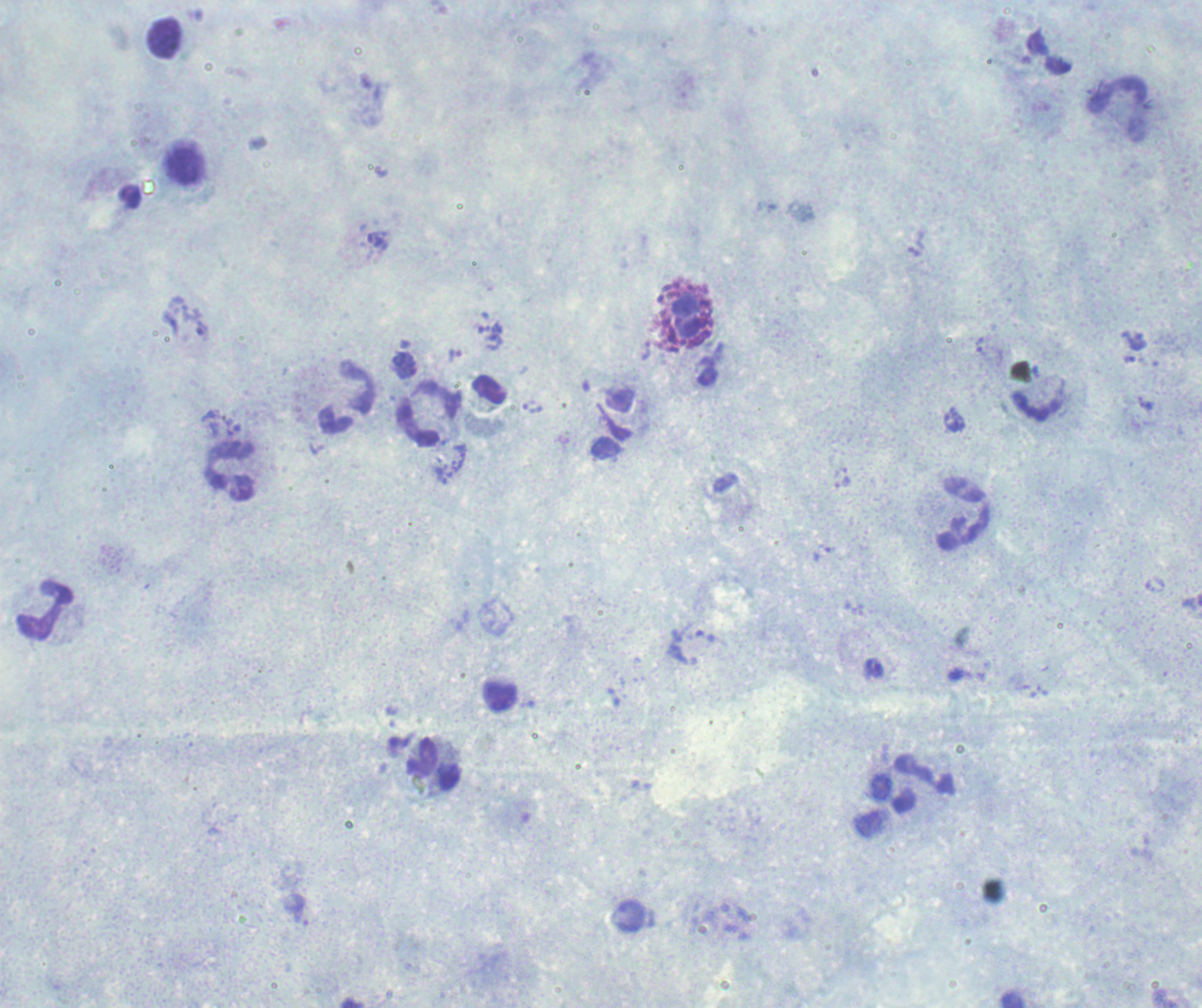 One field from this slide. Romanowsky-stained preparation. Image is 1202×1008 pixels. Thick smear of blood.